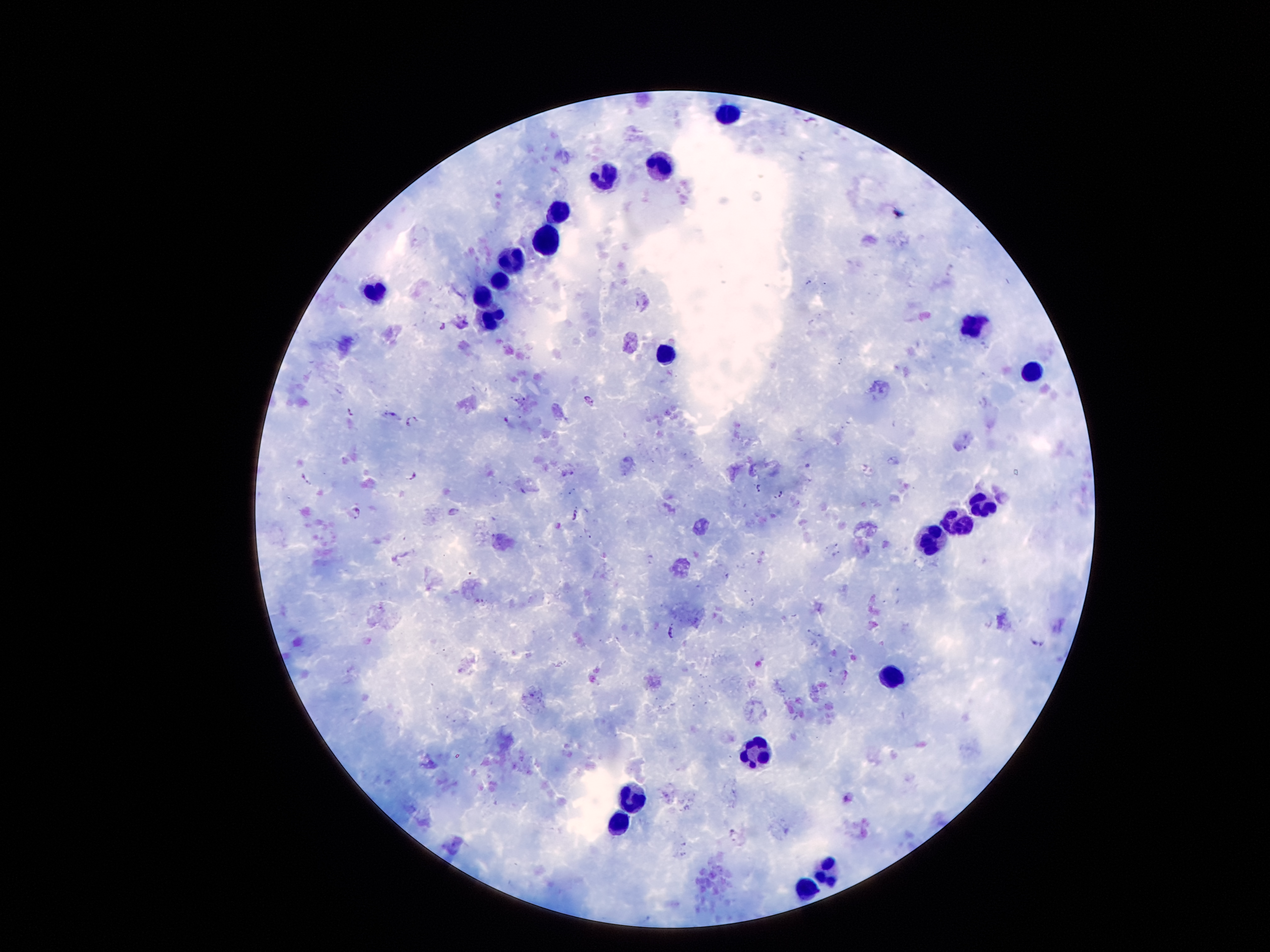

image_size: 1270×952 pixels
magnification: 100x
preparation: thick blood smear
stain: Giemsa
capture: smartphone camera through the microscope eyepiece
patient_malaria_status: positive for Plasmodium falciparum
field_of_view: one from this slide
leukocyte_locations: 'approximate object centers, in pixels from the top-left corner: (x=726, y=116), (x=662, y=165), (x=604, y=176), (x=558, y=213), (x=547, y=239), (x=511, y=264), (x=499, y=280), (x=376, y=294), (x=483, y=297), (x=498, y=319), (x=972, y=327), (x=663, y=357), (x=1029, y=372), (x=984, y=508), (x=961, y=522), (x=930, y=540), (x=892, y=676), (x=758, y=757), (x=631, y=797), (x=620, y=823), (x=827, y=873), (x=805, y=890)'
malaria_parasite_locations: 'approximate object centers, in pixels from the top-left corner: (x=592, y=400), (x=350, y=411), (x=409, y=422), (x=894, y=461), (x=413, y=476), (x=308, y=479), (x=760, y=488), (x=779, y=495), (x=357, y=512), (x=454, y=513), (x=574, y=517), (x=651, y=559), (x=672, y=632), (x=1038, y=640)'